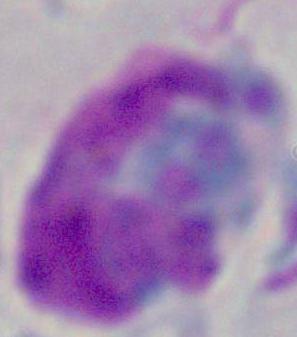
Summary:
  - Modality: photomicrograph
  - Magnification: 1000x
  - Identification: leukocyte